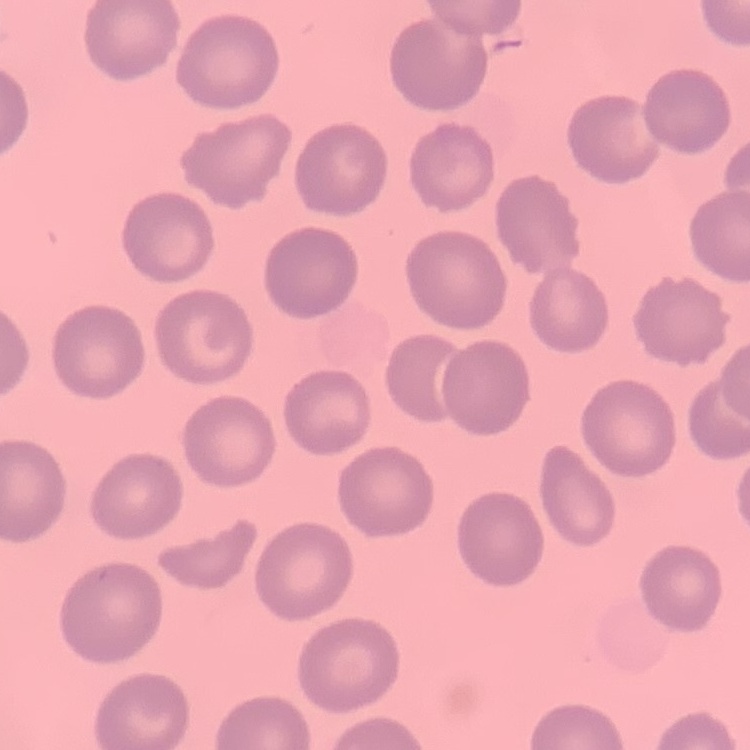
erythrocyte morphology = no rouleaux formation
preparation = thin blood film
stain = Field's or Giemsa
image type = one tile cut from a larger photomicrograph